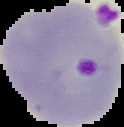 Result: malaria parasites detected. The area outside the segmented cell region is set to black. From a thin blood smear. Image is 124×127 pixels.